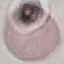 Result: no malaria parasites detected. Thin blood film. Giemsa stain. Automatically extracted cell patch, resized to 64 × 64 pixels. Photographed with a smartphone camera at the microscope eyepiece.